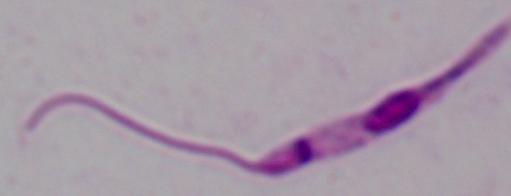

Summary:
  - Identification: Leishmania
  - Modality: micrograph
  - Magnification: 1000x